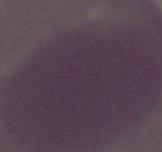
magnification = 1000x
identification = red blood cell
modality = micrograph